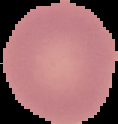
From a thin blood smear. Image is 118×124 pixels. The area outside the segmented cell region is set to black. Result: no malaria parasites detected.